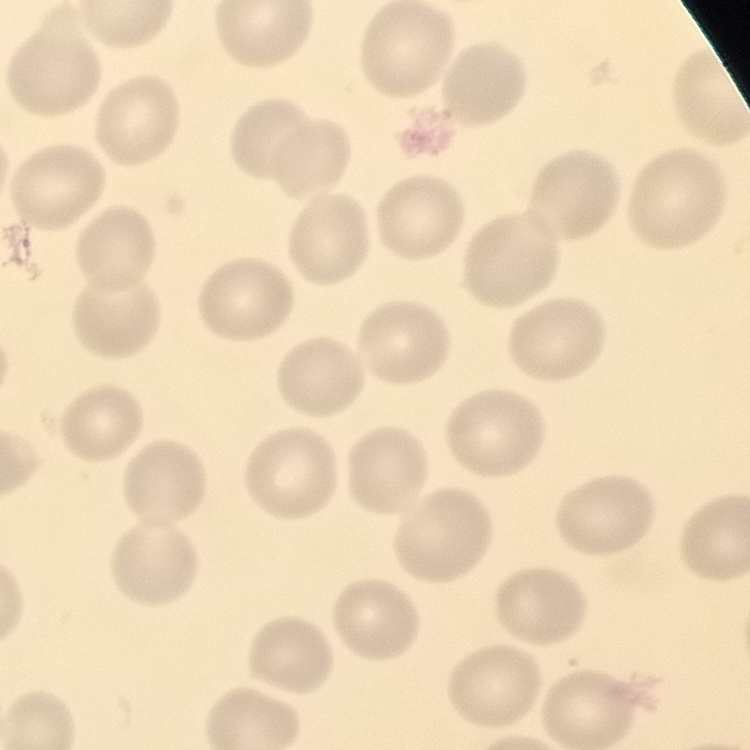 The erythrocytes show no rouleaux formation. Square crop of a larger photomicrograph. Thin blood film. Stained with either Field's or Giemsa.